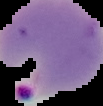
Summary:
  - Malaria status: parasitized
  - Image size: 103×106 pixels
  - Image type: segmented cell region on a black background
  - Preparation: thin blood film